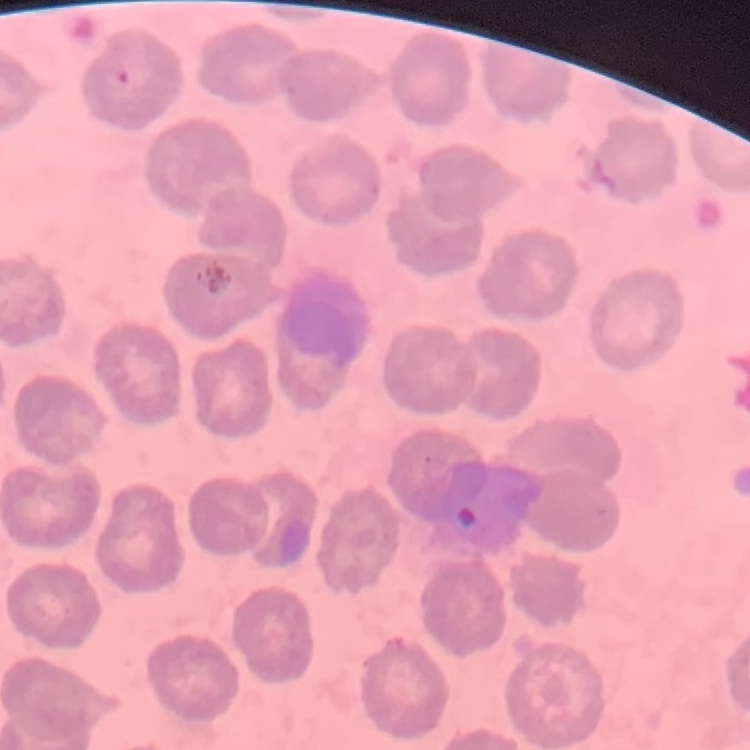
erythrocyte morphology = no rouleaux formation
image type = one tile cut from a larger photomicrograph
stain = Field's or Giemsa
preparation = thin blood film